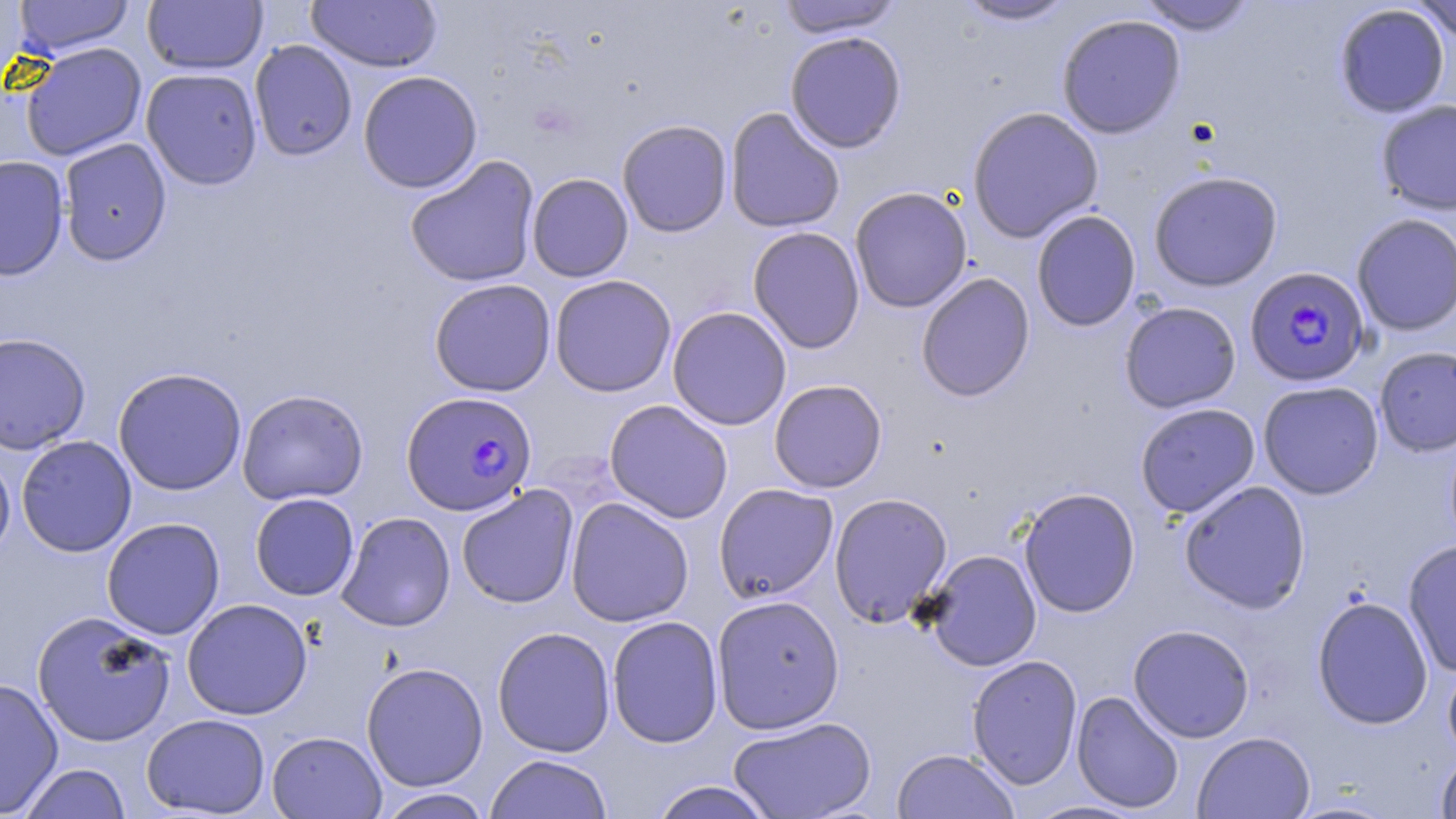

{
  "slide_level_diagnosis": "Plasmodium falciparum",
  "modality": "optical microscopy",
  "uninfected_red_blood_cell_locations": "approximate bounding boxes as (x1,y1)-(x2,y2) corner pairs in pixels: (0,0)-(30,86), (13,0)-(134,55), (143,0)-(267,75), (306,0)-(443,72), (954,0)-(1078,27), (1410,0)-(1456,43), (775,1)-(906,38), (1135,1)-(1259,35), (1334,4)-(1450,118), (1056,14)-(1186,140), (784,31)-(907,153), (249,40)-(358,161), (21,42)-(147,161), (141,68)-(263,190), (357,70)-(483,193), (1376,99)-(1456,215), (966,106)-(1104,244), (725,107)-(845,233), (617,119)-(733,238), (58,138)-(172,265), (0,155)-(69,281), (404,155)-(540,288), (1148,171)-(1283,291), (527,173)-(634,282), (849,186)-(972,313), (1031,209)-(1141,332), (1352,214)-(1456,336), (747,226)-(865,354), (916,272)-(1035,402), (549,274)-(677,397), (428,278)-(556,397), (1119,301)-(1241,413), (667,306)-(792,431), (0,332)-(91,454), (1374,346)-(1456,457), (113,367)-(247,496), (769,379)-(887,493), (1258,381)-(1384,500), (236,389)-(369,505), (604,399)-(733,523), (1135,402)-(1260,518), (16,435)-(137,557), (0,448)-(15,565), (1178,480)-(1311,614), (713,483)-(839,603), (456,485)-(579,609), (1018,487)-(1141,618), (828,492)-(953,627), (249,493)-(360,600), (565,497)-(694,627), (336,511)-(456,631), (101,517)-(225,639), (1403,538)-(1456,678), (923,549)-(1042,671), (711,594)-(845,734), (1311,595)-(1434,730), (181,598)-(313,720), (32,611)-(176,747), (607,615)-(723,748), (1128,624)-(1255,742), (492,626)-(616,757), (966,654)-(1083,791), (1443,657)-(1456,767), (361,662)-(489,791), (0,677)-(64,817), (1071,690)-(1185,814), (141,713)-(270,817), (728,715)-(877,819), (267,730)-(387,818), (1193,731)-(1315,818), (892,748)-(1020,819), (1435,751)-(1456,818), (485,754)-(613,819), (19,763)-(132,819), (648,781)-(776,819), (376,788)-(492,819), (1022,799)-(1152,818)",
  "preparation": "thin blood film",
  "stain": "May-Grünwald-Giemsa",
  "plasmodium_falciparum_infected_red_blood_cell_locations": "approximate bounding boxes as (x1,y1)-(x2,y2) corner pairs in pixels: (1244,265)-(1372,387), (401,390)-(538,515)",
  "magnification": "1000x",
  "field_of_view": "single",
  "image_size": "1456×819 pixels"
}